State which malaria species this is.
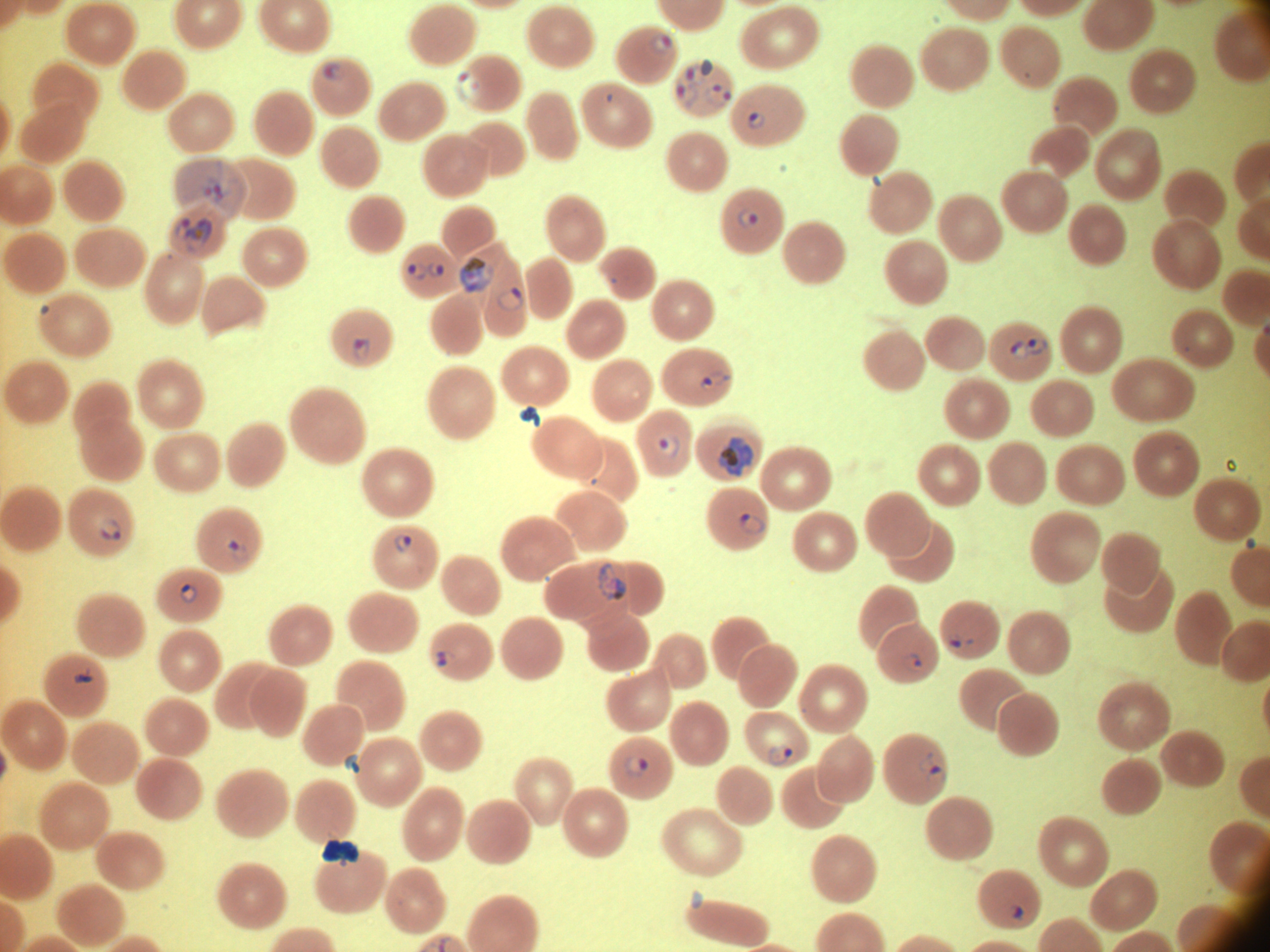
Plasmodium falciparum.

{
  "life_cycle_stages_among_the_annotated_parasites": "ring form, trophozoite",
  "stain": "Giemsa",
  "magnification": "100x",
  "field_of_view": "single",
  "ring_form_locations": "approximate bounding boxes as [x1, y1, x2, y2] in pixels, from the source annotation, which is not necessarily exhaustive: [650, 34, 672, 51], [323, 62, 345, 81], [686, 62, 707, 85], [457, 69, 480, 99], [676, 83, 700, 109], [707, 83, 732, 107], [747, 112, 765, 130], [738, 210, 757, 228], [408, 261, 428, 281], [428, 262, 445, 278], [497, 286, 524, 313], [41, 305, 49, 315], [353, 337, 371, 360], [1025, 338, 1048, 357], [1010, 340, 1027, 360], [700, 371, 731, 390], [658, 434, 681, 457], [740, 512, 765, 535], [98, 518, 122, 541], [393, 534, 412, 553], [228, 540, 249, 562], [179, 584, 198, 603], [945, 635, 962, 649], [436, 651, 456, 666], [904, 655, 926, 672], [73, 666, 93, 684], [769, 745, 792, 766], [918, 752, 934, 773], [623, 756, 648, 779], [926, 764, 948, 785], [1011, 906, 1023, 919]",
  "image_size": "1270×952 pixels",
  "preparation": "thin blood smear",
  "microscope": "Leica DM2000 with built-in camera",
  "trophozoite_locations": "approximate bounding boxes as [x1, y1, x2, y2] in pixels, from the source annotation, which is not necessarily exhaustive: [174, 160, 245, 218], [175, 218, 191, 242], [186, 219, 212, 253], [460, 257, 495, 293], [718, 435, 754, 477], [598, 561, 627, 601]"
}